Identify the parasite.
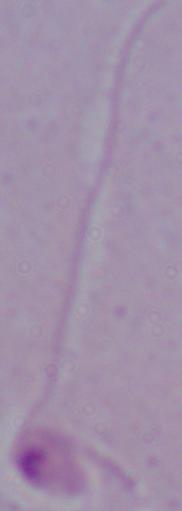

This is Leishmania.

magnification = 1000x
modality = photomicrograph